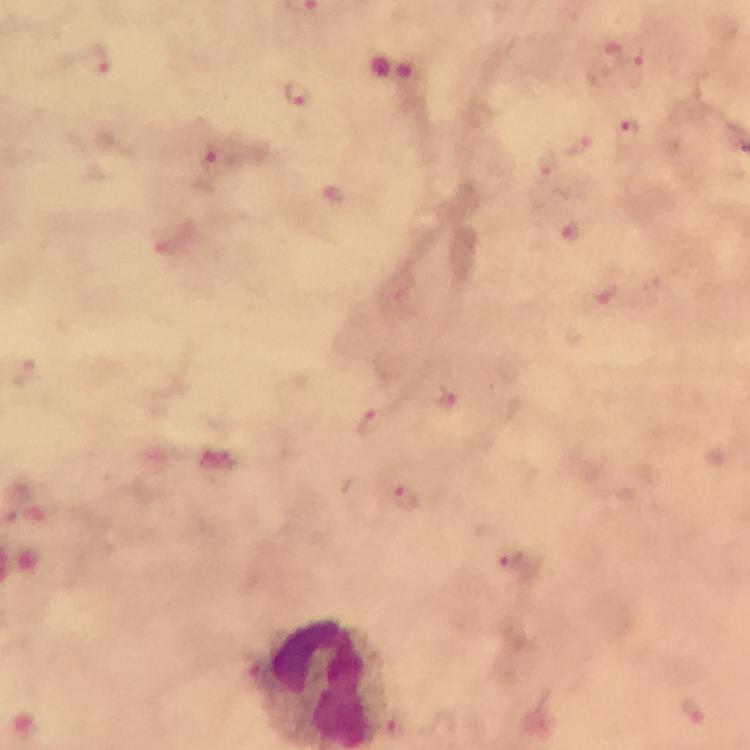

{
  "plasmodium_parasite_locations": "approximate centers as [x, y] in pixels: [628, 53], [91, 59], [300, 93], [628, 131], [450, 400], [360, 411], [406, 500], [514, 563]",
  "capture": "smartphone mounted on the microscope",
  "magnification": "100x",
  "cropped_from": "a single field of view",
  "image_size": "750×750 pixels",
  "preparation": "thick blood film",
  "stain": "Giemsa",
  "immersion_oil": "used",
  "context": "from a diagnostic examination for malaria"
}